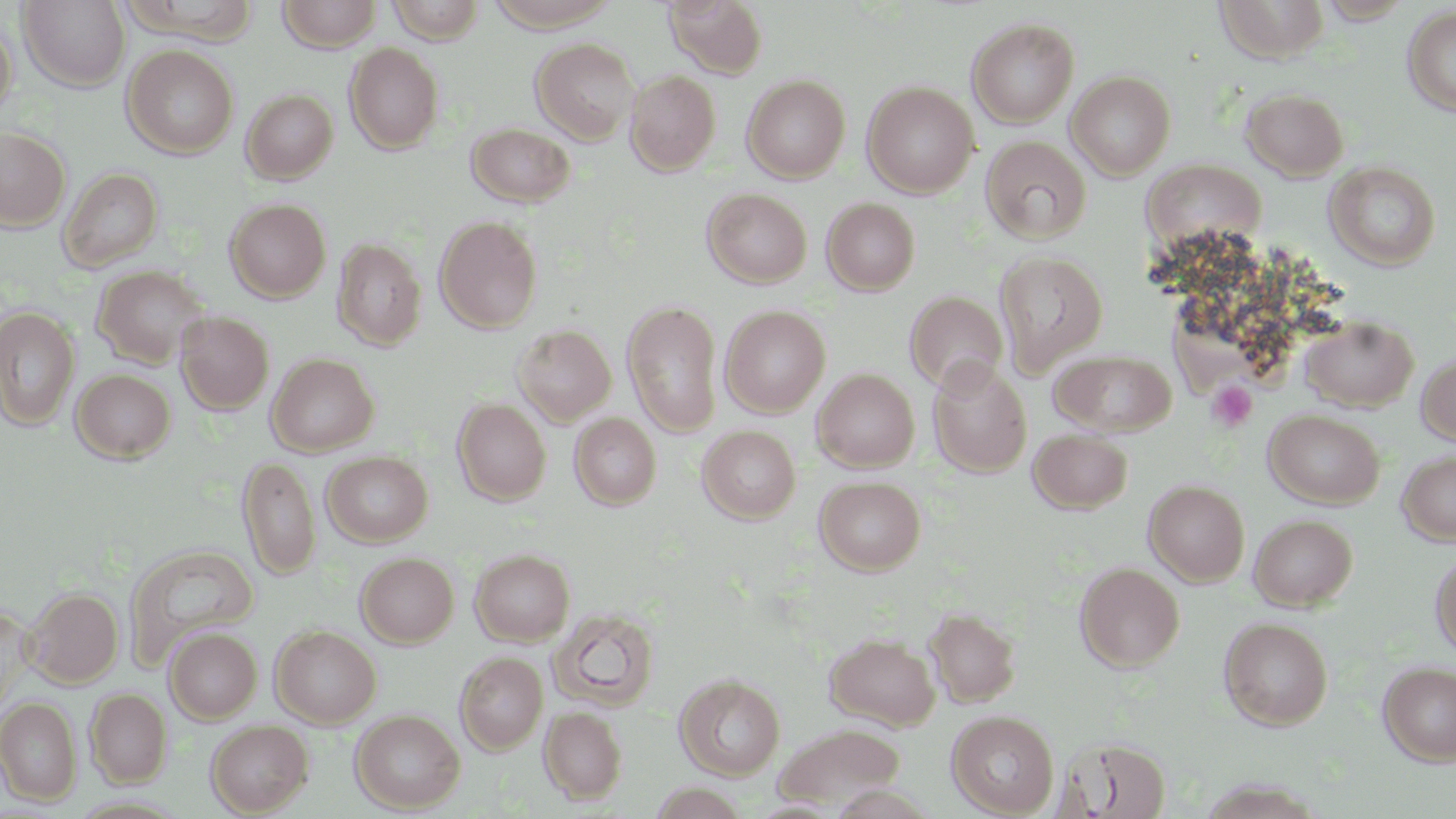
{
  "slide_level_diagnosis": "no evidence of blood parasites",
  "image_size": "1456×819 pixels",
  "modality": "light microscopy",
  "magnification": "1000x",
  "platelet_locations": "approximate bounding boxes as [x1, y1, x2, y2] in pixels: [1207, 381, 1257, 432]",
  "preparation": "thin blood film",
  "uninfected_red_blood_cell_locations": "approximate bounding boxes as [x1, y1, x2, y2] in pixels: [277, 0, 382, 51], [386, 0, 486, 43], [664, 0, 768, 78], [1214, 0, 1330, 62], [18, 1, 130, 91], [119, 1, 259, 42], [483, 1, 621, 32], [1402, 5, 1456, 117], [966, 17, 1079, 128], [0, 19, 17, 121], [530, 38, 639, 144], [345, 43, 444, 154], [122, 44, 239, 158], [625, 70, 721, 176], [1066, 70, 1176, 179], [742, 74, 850, 183], [862, 81, 979, 198], [241, 88, 339, 185], [1241, 88, 1349, 180], [466, 122, 575, 207], [0, 127, 70, 231], [980, 136, 1091, 243], [1144, 158, 1263, 248], [1325, 162, 1441, 270], [58, 167, 162, 272], [702, 188, 812, 287], [225, 198, 331, 302], [822, 198, 920, 295], [434, 215, 543, 333], [332, 238, 427, 350], [993, 250, 1108, 376], [92, 265, 210, 369], [905, 290, 1008, 394], [622, 299, 723, 437], [720, 305, 830, 416], [1, 306, 80, 431], [175, 311, 274, 415], [1301, 315, 1418, 411], [512, 324, 616, 426], [1051, 350, 1176, 436], [1417, 352, 1456, 446], [266, 353, 379, 456], [927, 359, 1032, 477], [812, 368, 920, 472], [71, 369, 175, 463], [452, 398, 551, 505], [1264, 409, 1384, 508], [569, 413, 661, 510], [697, 425, 801, 523], [1028, 429, 1132, 514], [1398, 450, 1456, 545], [321, 451, 433, 547], [238, 455, 320, 580], [814, 475, 926, 574], [1144, 480, 1250, 585], [1249, 514, 1357, 611], [125, 545, 259, 664], [470, 548, 575, 646], [1430, 551, 1456, 657], [356, 552, 459, 647], [1074, 562, 1184, 671], [24, 587, 123, 688], [0, 603, 35, 713], [924, 605, 1021, 708], [549, 607, 660, 711], [1219, 616, 1334, 730], [270, 625, 380, 728], [164, 627, 262, 723], [825, 632, 941, 731], [455, 651, 548, 754], [1378, 661, 1456, 765], [674, 673, 785, 780], [86, 688, 171, 787], [0, 697, 81, 804], [539, 706, 627, 804], [351, 709, 465, 812], [947, 710, 1059, 816], [206, 720, 313, 816], [774, 724, 905, 811], [1063, 737, 1172, 818]",
  "field_of_view": "single",
  "stain": "May-Grünwald-Giemsa"
}